Name the parasite shown.
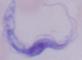
This is a trypanosome.

Summary:
  - Magnification: 1000x
  - Modality: micrograph